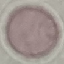

Summary:
  - Malaria status: uninfected
  - Image type: automatically extracted cell patch, resized to 64 × 64 pixels
  - Capture: smartphone through the microscope eyepiece
  - Stain: Giemsa
  - Preparation: thin blood smear